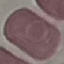
Summary:
  - Malaria status: uninfected
  - Stain: Giemsa
  - Image type: automatically extracted cell patch, resized to 64 × 64 pixels
  - Preparation: thin blood film
  - Capture: smartphone camera at the microscope eyepiece